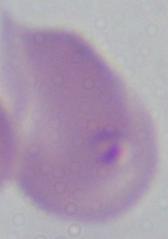
Summary:
  - Magnification: 1000x
  - Identification: Babesia
  - Modality: micrograph